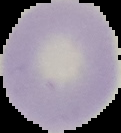

result = no malaria parasites seen
image type = segmented cell region with the area outside set to black
image size = 121×133 pixels
preparation = thin blood smear